State which parasite is depicted.
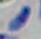

Toxoplasma gondii.

Photomicrograph. Captured at 1000x magnification.